Assess the morphology of the erythrocytes.
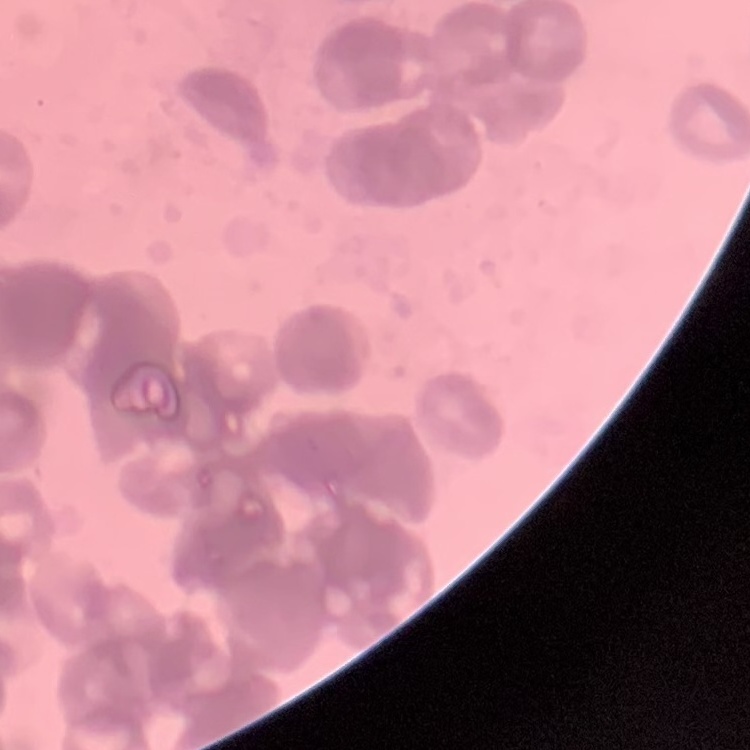

They show rouleaux formation.

preparation = thin peripheral smear
stain = Field's or Giemsa
image type = one tile cut from a larger photomicrograph